Locate every blood parasite and identify its species.
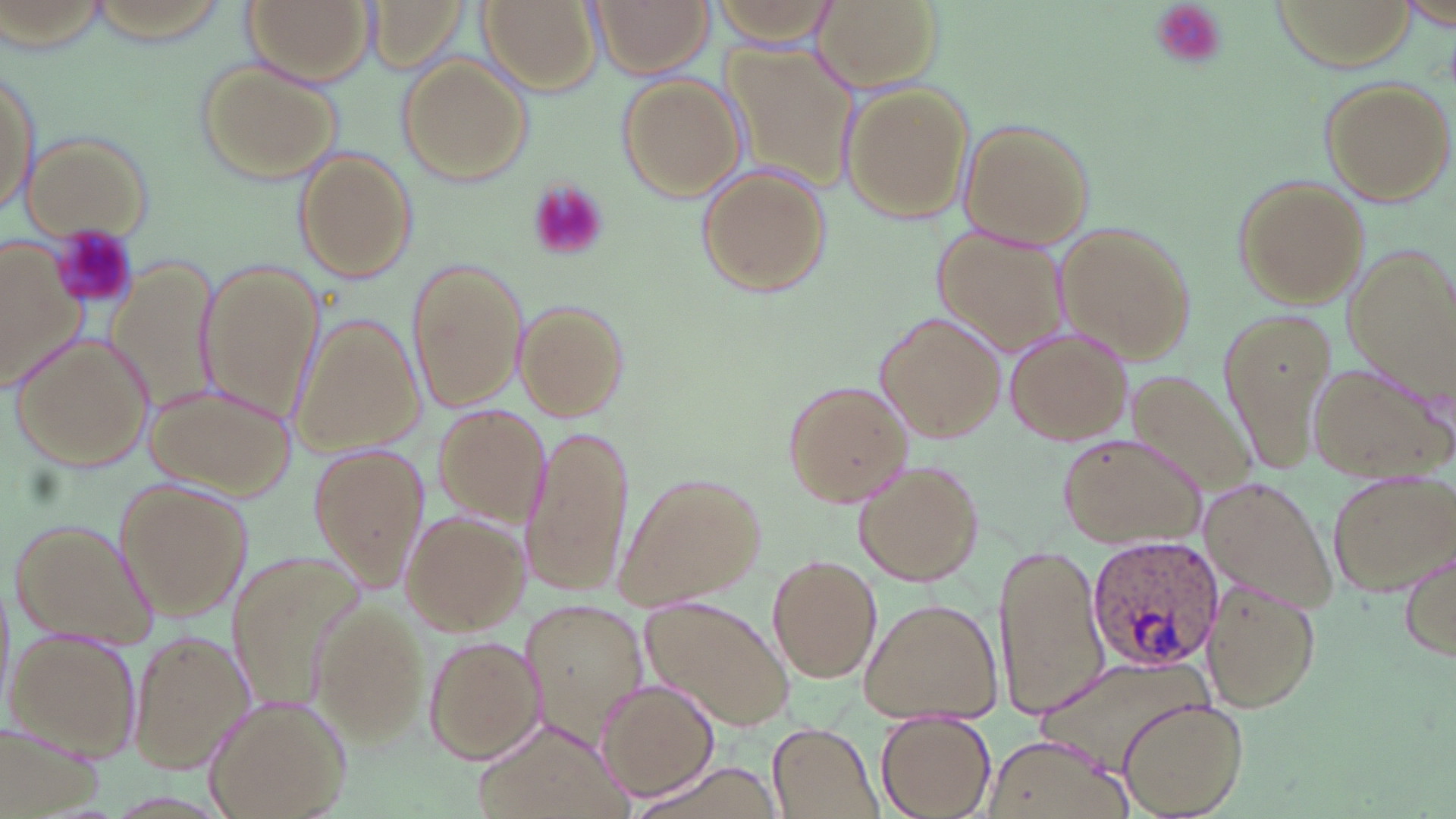

Approximate bounding boxes as named x1/y1/x2/y2 corners in pixels.
Plasmodium ovale-infected red blood cells: (x1=1086, y1=536, x2=1224, y2=670).
No Plasmodium falciparum, Plasmodium malariae, Plasmodium vivax, Babesia divergens, or Trypanosoma brucei observed.

slide-level diagnosis = Plasmodium ovale
magnification = 1000x
modality = optical microscopy
image size = 1456×819 pixels
uninfected red blood cell locations = approximate bounding boxes as named x1/y1/x2/y2 corners in pixels: (x1=243, y1=0, x2=372, y2=85), (x1=362, y1=0, x2=473, y2=75), (x1=480, y1=0, x2=600, y2=96), (x1=591, y1=0, x2=711, y2=77), (x1=710, y1=0, x2=842, y2=46), (x1=811, y1=0, x2=946, y2=96), (x1=1397, y1=1, x2=1456, y2=29), (x1=725, y1=44, x2=860, y2=185), (x1=397, y1=54, x2=535, y2=185), (x1=2, y1=59, x2=40, y2=222), (x1=196, y1=59, x2=342, y2=186), (x1=621, y1=75, x2=746, y2=201), (x1=1320, y1=77, x2=1453, y2=208), (x1=839, y1=82, x2=974, y2=224), (x1=958, y1=120, x2=1096, y2=251), (x1=19, y1=131, x2=151, y2=242), (x1=292, y1=149, x2=415, y2=284), (x1=697, y1=165, x2=830, y2=296), (x1=1231, y1=175, x2=1369, y2=310), (x1=1056, y1=222, x2=1195, y2=364), (x1=932, y1=227, x2=1071, y2=362), (x1=0, y1=235, x2=88, y2=395), (x1=1340, y1=248, x2=1456, y2=404), (x1=106, y1=258, x2=223, y2=415), (x1=407, y1=258, x2=528, y2=413), (x1=198, y1=261, x2=324, y2=424), (x1=513, y1=300, x2=626, y2=422), (x1=1213, y1=306, x2=1337, y2=474), (x1=874, y1=313, x2=1005, y2=444), (x1=289, y1=315, x2=425, y2=458), (x1=1003, y1=325, x2=1132, y2=447), (x1=9, y1=333, x2=155, y2=471), (x1=1310, y1=363, x2=1448, y2=483), (x1=1113, y1=368, x2=1262, y2=506), (x1=143, y1=380, x2=296, y2=498), (x1=782, y1=380, x2=913, y2=508), (x1=429, y1=405, x2=549, y2=528), (x1=521, y1=424, x2=633, y2=597), (x1=1056, y1=434, x2=1204, y2=547), (x1=306, y1=443, x2=430, y2=591), (x1=854, y1=461, x2=985, y2=585), (x1=1329, y1=470, x2=1456, y2=594), (x1=615, y1=471, x2=767, y2=614), (x1=1199, y1=480, x2=1335, y2=612), (x1=115, y1=481, x2=252, y2=624), (x1=400, y1=512, x2=525, y2=634), (x1=11, y1=516, x2=157, y2=648), (x1=996, y1=540, x2=1112, y2=721), (x1=1398, y1=545, x2=1456, y2=665), (x1=768, y1=554, x2=880, y2=680), (x1=229, y1=557, x2=358, y2=713), (x1=1201, y1=577, x2=1322, y2=713), (x1=860, y1=596, x2=1001, y2=722), (x1=520, y1=598, x2=649, y2=748), (x1=639, y1=598, x2=793, y2=732), (x1=314, y1=605, x2=432, y2=743), (x1=7, y1=627, x2=142, y2=762), (x1=127, y1=631, x2=253, y2=773), (x1=424, y1=636, x2=542, y2=764), (x1=599, y1=682, x2=720, y2=802), (x1=204, y1=695, x2=352, y2=819), (x1=1119, y1=697, x2=1248, y2=818), (x1=875, y1=717, x2=996, y2=819), (x1=470, y1=718, x2=633, y2=818), (x1=3, y1=719, x2=101, y2=819), (x1=767, y1=725, x2=883, y2=819), (x1=987, y1=736, x2=1129, y2=819), (x1=622, y1=759, x2=784, y2=818)
field of view = one of a larger specimen
platelet locations = approximate bounding boxes as named x1/y1/x2/y2 corners in pixels: (x1=1148, y1=1, x2=1228, y2=71), (x1=525, y1=178, x2=610, y2=263), (x1=52, y1=228, x2=140, y2=312)
stain = May-Grünwald-Giemsa
preparation = thin blood smear